Report the malaria status.
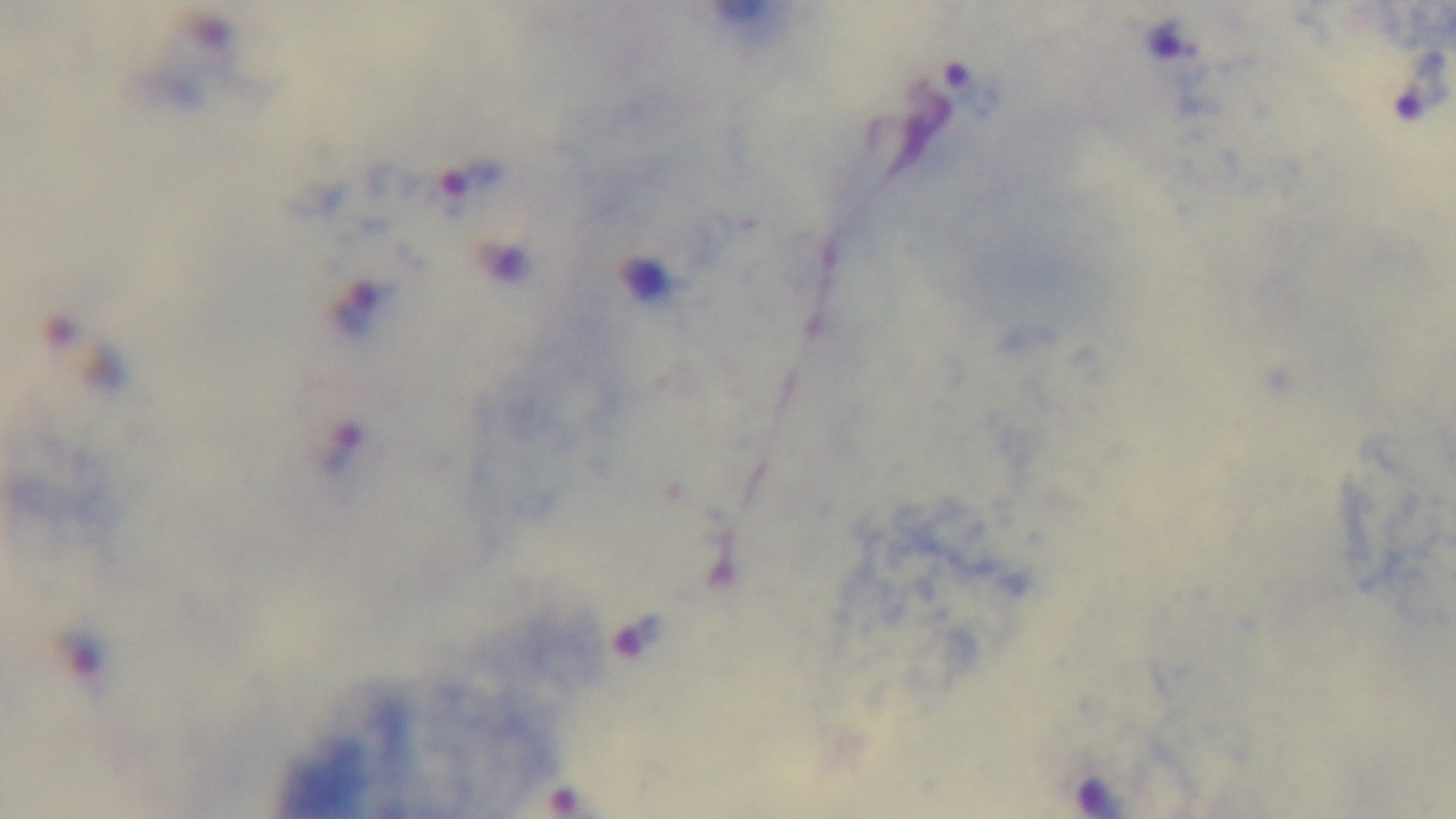
Infected.

{
  "modality": "light microscopy",
  "preparation": "thick",
  "objective": "100x oil immersion",
  "field_of_view": "one from the slide",
  "capture": "mounted 4K digital camera",
  "stain": "Giemsa"
}